State which cell type is depicted.
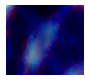

A leukocyte.

Captured at 1000x magnification. Photomicrograph.